Report the malaria status of this cell.
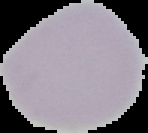
It is uninfected.

The area outside the segmented cell region is set to black. Image is 148×133 pixels. From a thin blood film.